Outline each blood parasite and name the species.
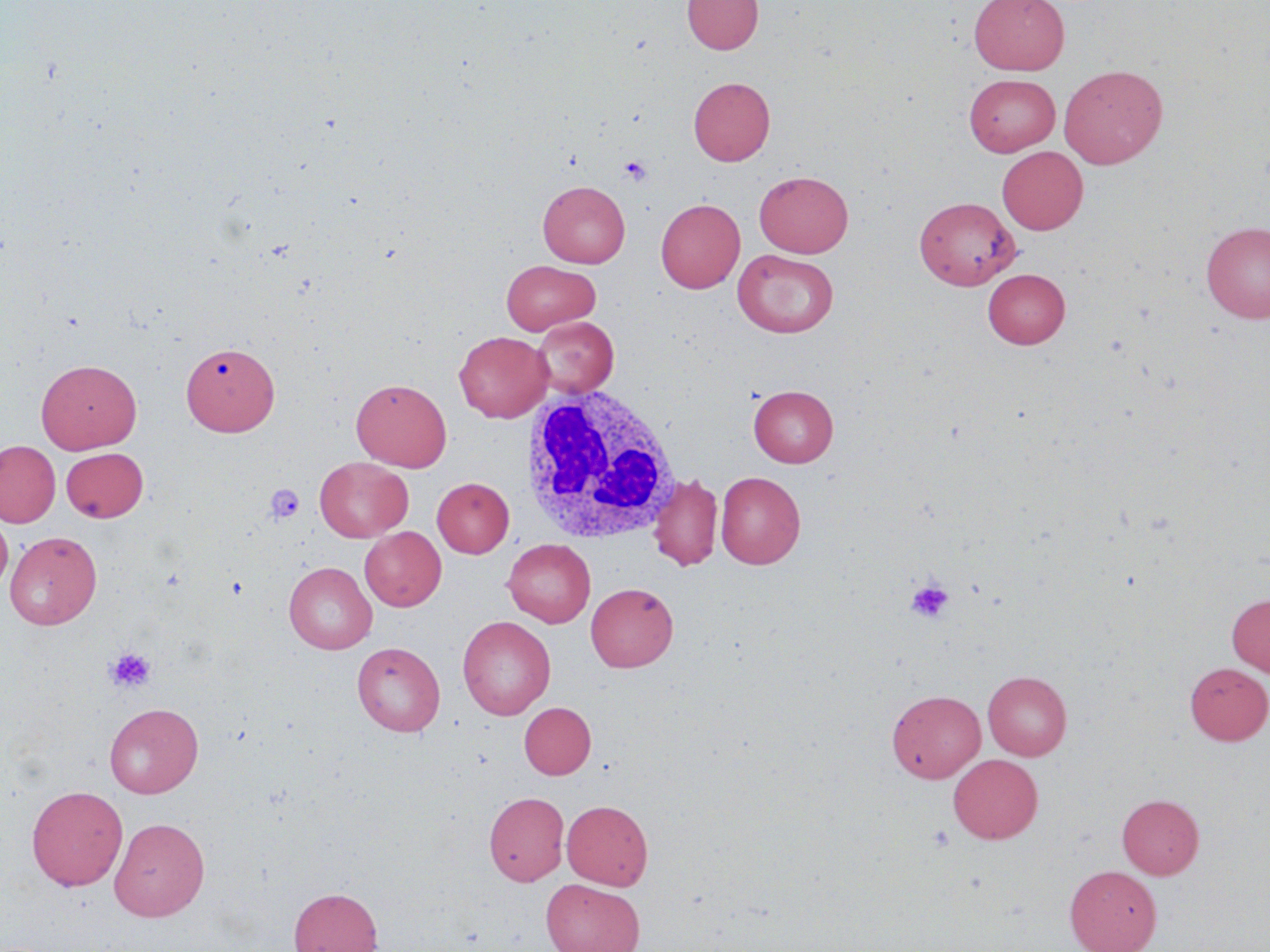
No blood parasites observed.

{
  "slide_level_diagnosis": "negative for blood parasites",
  "preparation": "thin blood smear",
  "modality": "light microscopy",
  "platelet_locations": "approximate bounding boxes as named x1/y1/x2/y2 corners in pixels: (x1=619, y1=156, x2=652, y2=186), (x1=264, y1=484, x2=306, y2=523), (x1=905, y1=579, x2=954, y2=623), (x1=106, y1=646, x2=157, y2=693)",
  "image_size": "1270×952 pixels",
  "magnification": "1000x",
  "uninfected_red_blood_cell_locations": "approximate bounding boxes as named x1/y1/x2/y2 corners in pixels: (x1=682, y1=0, x2=763, y2=54), (x1=970, y1=0, x2=1070, y2=75), (x1=1058, y1=64, x2=1168, y2=169), (x1=964, y1=73, x2=1060, y2=156), (x1=688, y1=77, x2=775, y2=166), (x1=997, y1=146, x2=1088, y2=234), (x1=754, y1=171, x2=853, y2=257), (x1=537, y1=180, x2=630, y2=268), (x1=914, y1=196, x2=1020, y2=290), (x1=655, y1=198, x2=745, y2=293), (x1=1201, y1=221, x2=1270, y2=323), (x1=733, y1=250, x2=838, y2=338), (x1=502, y1=260, x2=600, y2=335), (x1=982, y1=268, x2=1070, y2=348), (x1=532, y1=316, x2=619, y2=397), (x1=453, y1=331, x2=553, y2=423), (x1=181, y1=342, x2=279, y2=436), (x1=36, y1=359, x2=142, y2=453), (x1=351, y1=378, x2=451, y2=471), (x1=749, y1=385, x2=838, y2=467), (x1=0, y1=440, x2=61, y2=527), (x1=61, y1=448, x2=149, y2=522), (x1=314, y1=457, x2=413, y2=541), (x1=716, y1=471, x2=805, y2=568), (x1=649, y1=474, x2=722, y2=571), (x1=432, y1=477, x2=514, y2=557), (x1=0, y1=516, x2=13, y2=595), (x1=360, y1=526, x2=446, y2=611), (x1=5, y1=531, x2=102, y2=629), (x1=503, y1=538, x2=595, y2=627), (x1=283, y1=561, x2=377, y2=653), (x1=585, y1=582, x2=678, y2=672), (x1=1227, y1=593, x2=1270, y2=677), (x1=457, y1=615, x2=555, y2=719), (x1=352, y1=641, x2=445, y2=736), (x1=1185, y1=662, x2=1270, y2=744), (x1=982, y1=671, x2=1072, y2=761), (x1=886, y1=689, x2=986, y2=783), (x1=105, y1=702, x2=203, y2=798), (x1=519, y1=702, x2=596, y2=779), (x1=948, y1=753, x2=1043, y2=843), (x1=26, y1=785, x2=128, y2=891), (x1=484, y1=792, x2=569, y2=885), (x1=1117, y1=794, x2=1204, y2=879), (x1=562, y1=800, x2=653, y2=889), (x1=109, y1=817, x2=210, y2=921), (x1=1064, y1=865, x2=1162, y2=952), (x1=541, y1=879, x2=645, y2=952), (x1=289, y1=886, x2=383, y2=952)",
  "field_of_view": "one of a larger specimen",
  "white_blood_cell_locations": "approximate bounding boxes as named x1/y1/x2/y2 corners in pixels: (x1=519, y1=383, x2=682, y2=546)",
  "stain": "May-Grünwald-Giemsa"
}